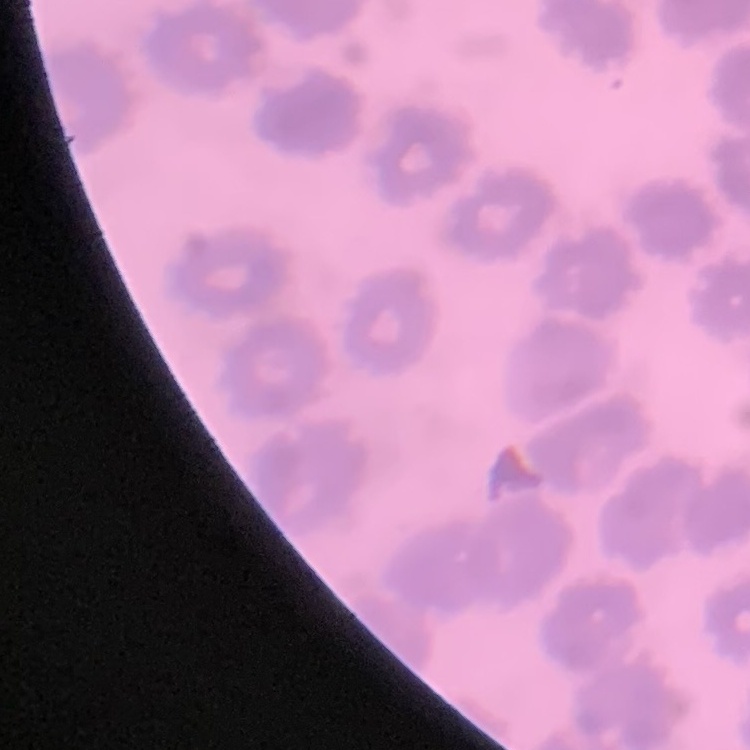

Summary:
  - Red blood cell morphology: no rouleaux formation
  - Image type: square crop of a larger photomicrograph
  - Stain: Field's or Giemsa
  - Preparation: thin blood film